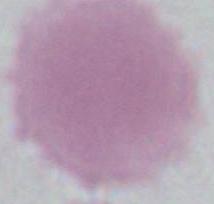

Micrograph. An erythrocyte is seen. Captured at 1000x magnification.